Identify the parasite.
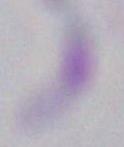

Toxoplasma gondii.

magnification = 1000x
modality = micrograph